Assess this cell for malaria.
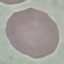
Uninfected.

Giemsa-stained preparation. Automatically extracted cell patch, resized to 64 × 64 pixels. Thin blood film. Photographed with a smartphone camera at the microscope eyepiece.